Assess this cell for malaria.
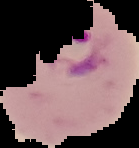
It is parasitized.

Image is 139×148 pixels. From a thin blood film. The area outside the segmented cell region is set to black.